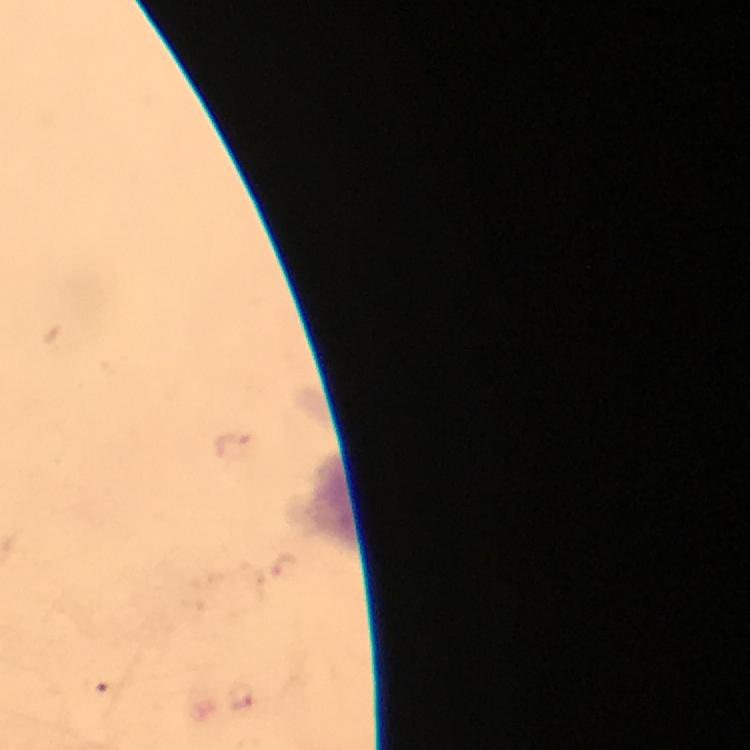 Approximate centers as [x, y] in pixels. Malaria parasite locations: [240, 694]. Photographed with a smartphone mounted on the microscope. 100x magnification. From a diagnostic examination for malaria. Image is 750×750 pixels. Thick blood film. Immersion oil was used. Giemsa-stained preparation. Cropped region of a single field of view.